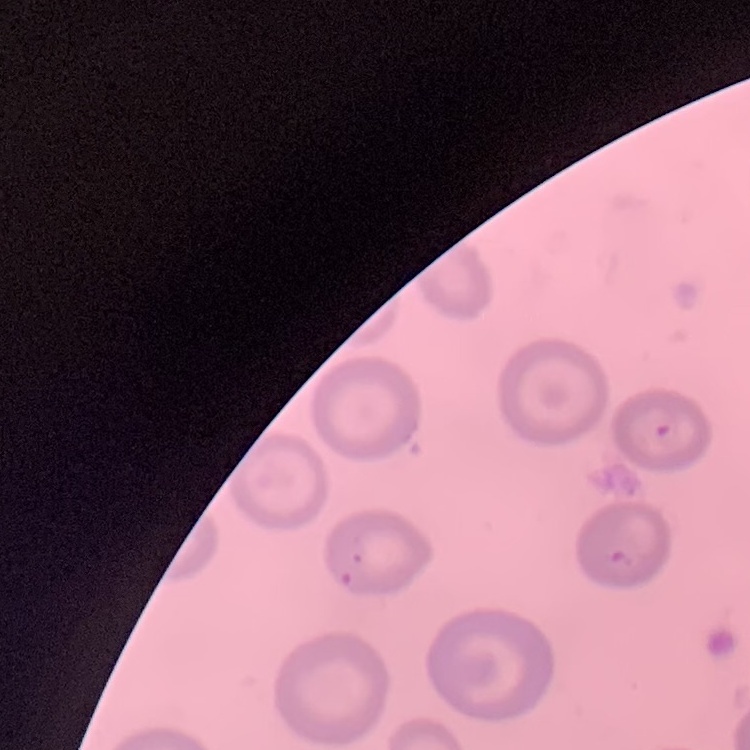
The erythrocytes exhibit no rouleaux formation. Thin blood film. Stained with either Field's or Giemsa. Square crop of a larger photomicrograph.